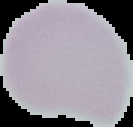
Summary:
  - Image size: 133×127 pixels
  - Malaria status: uninfected
  - Image type: segmented cell region on a black background
  - Preparation: thin blood smear